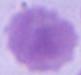
Summary:
  - Identification: erythrocyte
  - Magnification: 1000x
  - Modality: micrograph